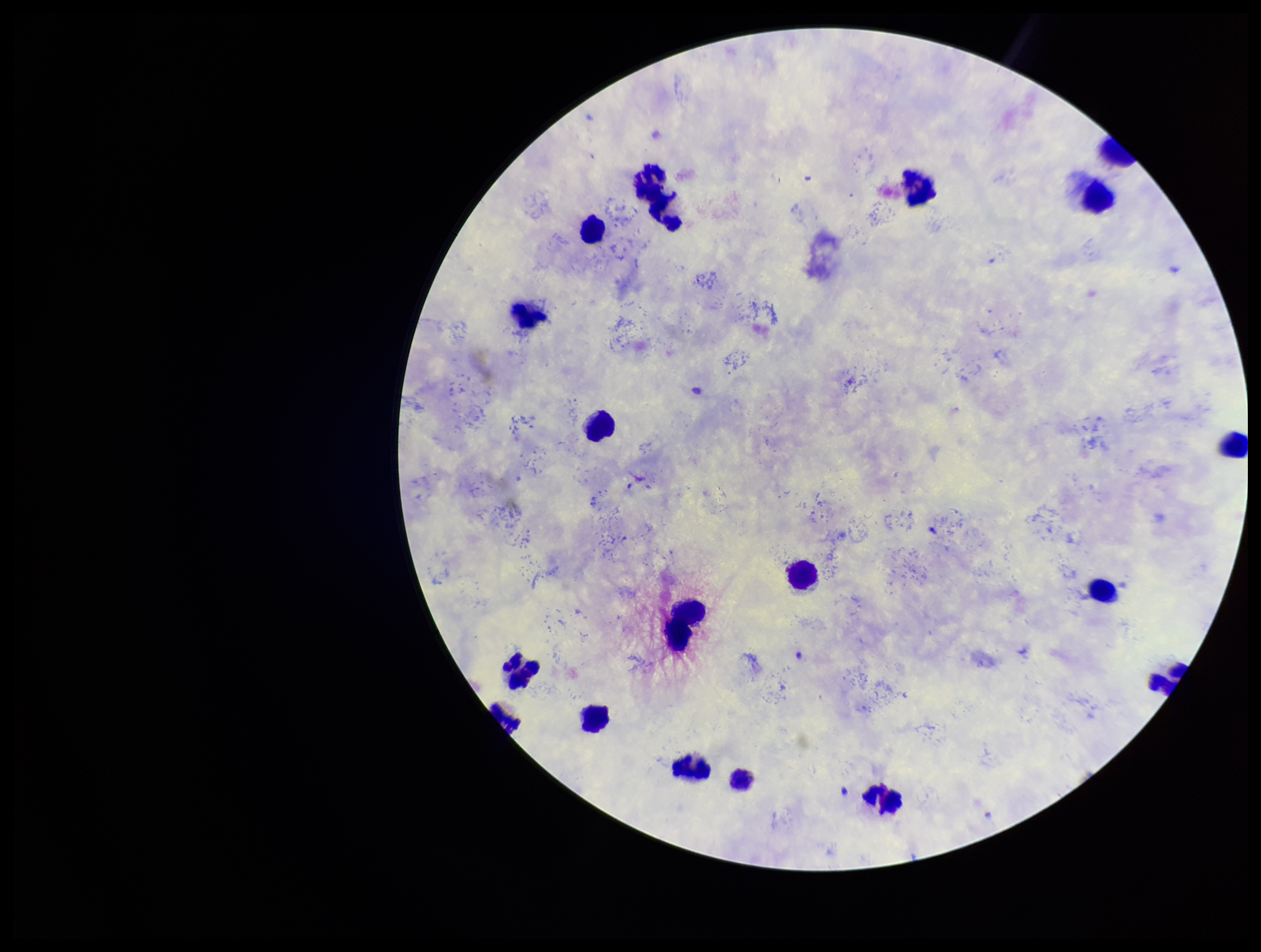

field of view = single
species reported for this patient = Plasmodium vivax
stain = Giemsa
patient malaria status = positive
parasite count = 0
Plasmodium parasites = none seen
preparation = thick blood smear
image size = 1261×952 pixels
leukocyte count = 20
capture = smartphone photograph through the microscope eyepiece